Locate the cells, classifying each as a parasitized red blood cell, an uninfected red blood cell, or a white blood cell.
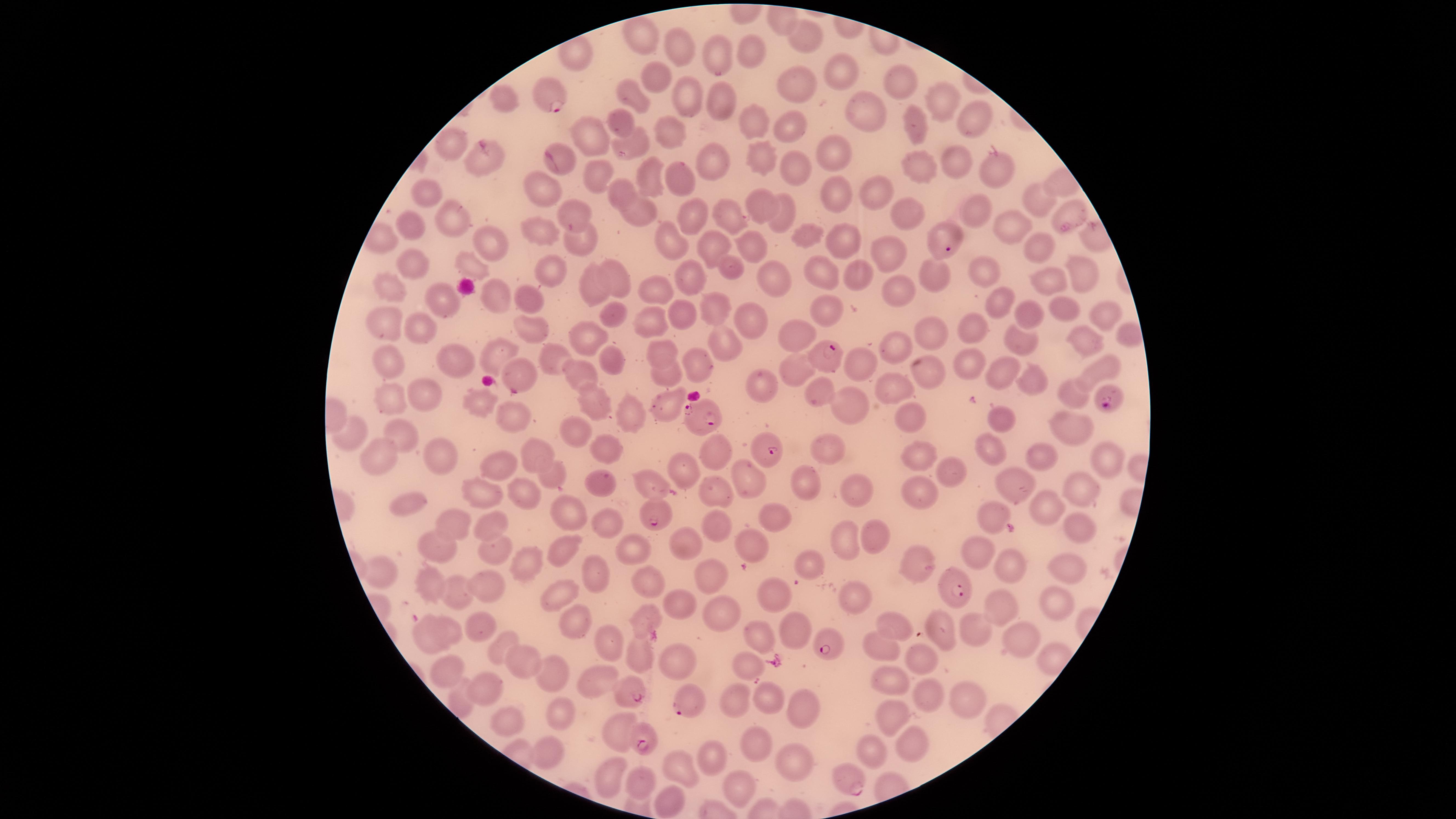

Approximate marker points as (x, y) in pixels.
Parasitized red blood cells: (550, 98), (947, 241), (828, 356), (1111, 402), (705, 410), (770, 447), (657, 514), (955, 590), (826, 641), (634, 693), (689, 701), (640, 742), (849, 785).
Uninfected red blood cells: (645, 37), (802, 38), (683, 49), (749, 50), (719, 56), (654, 76), (845, 79), (900, 81), (799, 87), (683, 92), (631, 96), (504, 99), (940, 100), (720, 103), (860, 114), (618, 120), (971, 121), (755, 126), (790, 126), (919, 130), (672, 132), (588, 135), (632, 144), (453, 147), (832, 150), (760, 154), (715, 158), (563, 162), (956, 162), (483, 168), (992, 168), (794, 169), (917, 170), (594, 173), (680, 177), (648, 179), (620, 188), (875, 189), (428, 197), (836, 197), (549, 200), (1038, 201), (760, 204), (785, 210), (979, 211), (1070, 211), (634, 213), (901, 215), (575, 216), (692, 218), (726, 218), (448, 219), (1004, 222), (406, 224), (545, 230), (669, 235), (839, 237), (803, 239), (1032, 240), (486, 242), (748, 242), (580, 243), (718, 244), (891, 250), (469, 264), (413, 265), (551, 272), (986, 273), (1074, 273), (734, 274), (931, 275), (819, 276), (854, 277), (614, 279), (692, 279), (771, 280), (387, 283), (597, 283), (658, 286), (1036, 288), (899, 291), (494, 296), (524, 301), (446, 302), (1003, 302), (1065, 309), (720, 310), (1029, 312), (1102, 312), (614, 314), (831, 316), (686, 317), (752, 318), (650, 323), (394, 325), (975, 330), (530, 331), (796, 333), (1129, 334), (426, 336), (930, 340), (584, 342), (1018, 342), (1084, 344), (723, 347), (663, 348), (893, 350), (499, 356), (551, 357), (614, 360), (462, 363), (973, 363), (394, 365), (705, 366), (927, 369), (859, 370), (998, 370), (1097, 370), (520, 371), (797, 371), (578, 374), (666, 376), (1029, 381), (762, 384), (892, 387), (421, 392), (1069, 392), (822, 393), (592, 396), (390, 400), (856, 401), (482, 404), (661, 405), (518, 413), (630, 415), (912, 417), (1004, 417), (1069, 423), (571, 434), (402, 437), (352, 443), (614, 448), (829, 451), (984, 451), (535, 453), (719, 454), (1043, 454), (919, 456), (1104, 457), (378, 458), (440, 460), (501, 464), (682, 470), (951, 472), (552, 474), (745, 479), (1018, 480), (595, 482), (647, 483), (807, 483), (853, 485), (1081, 487), (711, 492), (483, 493), (921, 493), (523, 495), (399, 508), (1048, 510), (571, 515), (770, 515), (996, 516), (493, 523), (717, 524), (610, 525), (453, 526), (1074, 526), (878, 536), (841, 538), (758, 544), (978, 546), (687, 547), (562, 549), (627, 549), (444, 550), (490, 550), (527, 563), (808, 564), (1012, 565), (1054, 565), (916, 571), (381, 574), (710, 577), (591, 580), (652, 583), (436, 586), (488, 586), (776, 590), (1055, 595), (463, 596), (562, 597), (858, 599), (683, 606), (1005, 607), (719, 610), (648, 620), (574, 622), (941, 623), (971, 625), (896, 627), (449, 629), (793, 630), (481, 633), (761, 636), (1020, 637), (428, 641), (603, 642), (883, 648), (497, 654), (636, 655), (921, 655), (675, 658), (514, 664), (745, 664), (448, 669), (547, 670), (890, 679), (601, 681), (483, 691), (927, 696), (455, 699), (963, 699), (737, 700), (769, 701), (805, 711), (560, 712), (898, 715), (505, 722), (619, 734), (912, 737), (759, 741), (872, 749), (549, 754), (712, 761), (793, 761), (678, 767), (614, 777), (644, 777), (739, 790), (671, 799).
No white blood cells identified.

Summary:
  - Field of view: single
  - Species: Plasmodium falciparum
  - Preparation: thin blood smear
  - Stain: Giemsa
  - Image size: 1456×819 pixels
  - Capture: smartphone photograph through the microscope eyepiece
  - Visible region: circular